Report the malaria status of this cell.
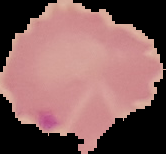

It is parasitized.

From a thin blood film. The area outside the segmented cell region is set to black. Image is 166×154 pixels.